Give the position of every Plasmodium parasite visible.
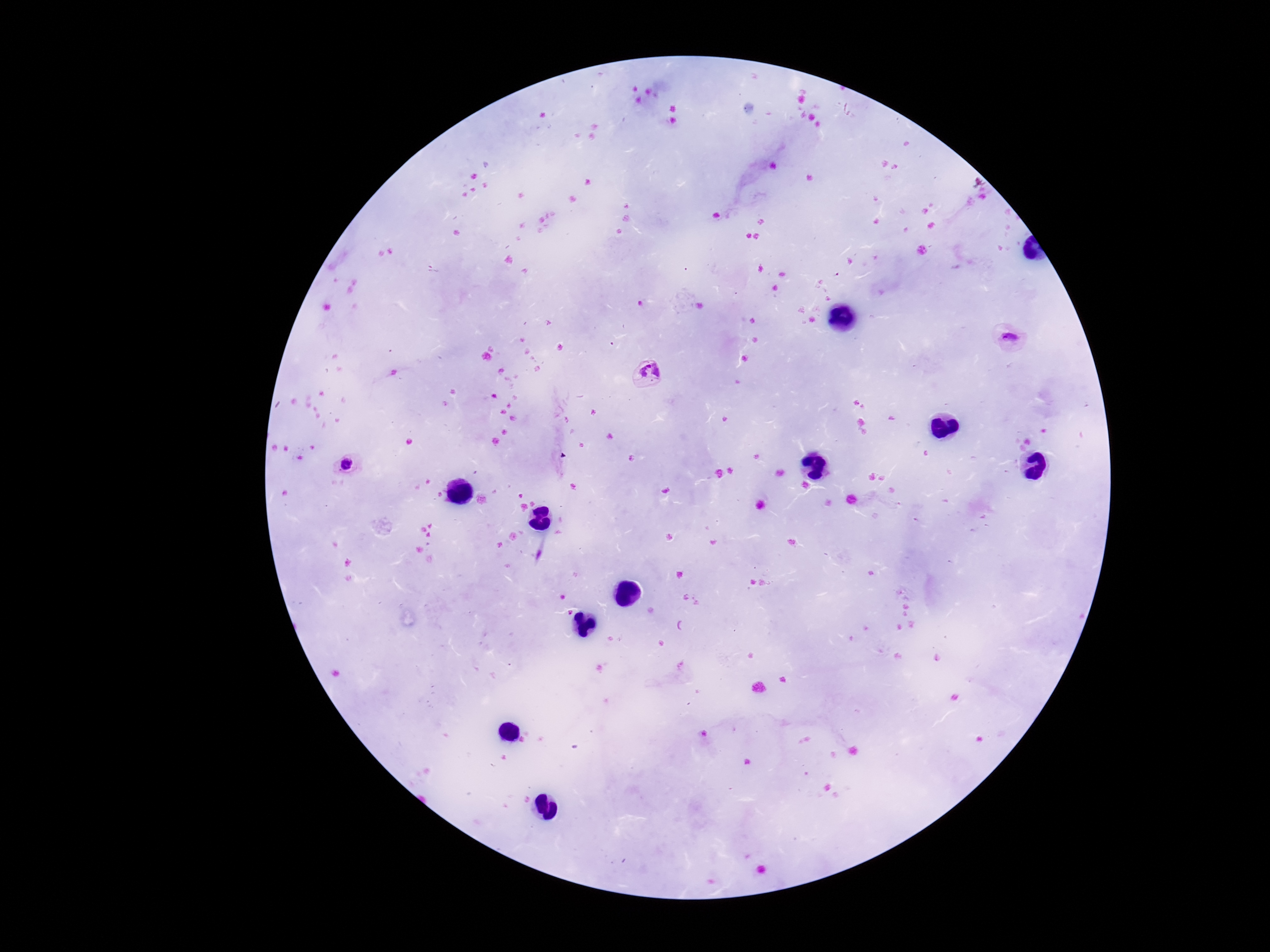
Approximate object centers, in pixels from the top-left corner.
Plasmodium parasites: (x=1009, y=338), (x=647, y=374), (x=346, y=464).

Smartphone photograph taken through the microscope eyepiece. Image is 1270×952 pixels. Patient malaria status: infected. Single field of view. 100x magnification. Thick blood smear. Giemsa-stained preparation.